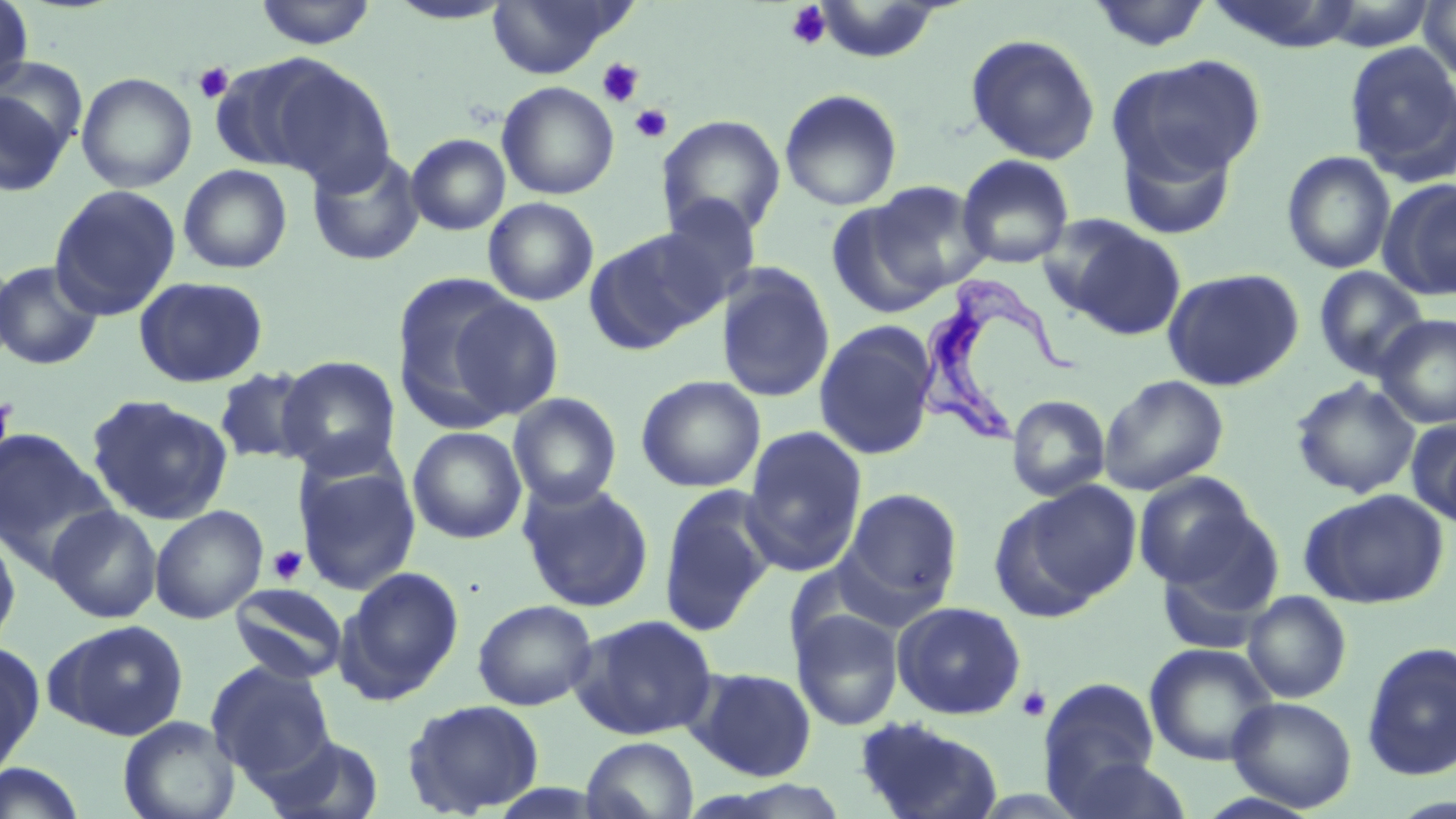
Approximate bounding boxes as (x1,y1)-(x2,y2) corner pairs in pixels. Platelet locations: (784,2)-(832,51), (597,57)-(644,107), (193,62)-(234,103), (630,104)-(672,143), (0,391)-(15,463), (266,545)-(308,586), (1016,686)-(1051,722). Trypanosoma brucei locations: (911,271)-(1082,446). Uninfected red blood cell locations: (1,0)-(34,95), (811,0)-(948,63), (1088,0)-(1214,53), (1418,0)-(1456,81), (254,1)-(377,49), (385,1)-(516,25), (486,1)-(631,79), (1315,1)-(1438,50), (964,33)-(1101,165), (1343,41)-(1456,185), (237,53)-(395,189), (1111,54)-(1266,185), (76,72)-(197,193), (497,81)-(620,200), (0,83)-(73,198), (779,88)-(903,211), (657,115)-(787,240), (1115,126)-(1240,241), (405,133)-(511,236), (307,148)-(425,267), (1281,151)-(1397,274), (957,154)-(1074,268), (178,164)-(293,274), (861,178)-(989,298), (1379,178)-(1456,301), (48,185)-(181,320), (656,193)-(763,311), (482,197)-(599,306), (823,197)-(952,320), (1048,217)-(1188,339), (584,228)-(719,354), (0,253)-(18,370), (0,261)-(104,371), (717,263)-(836,404), (1314,265)-(1430,380), (1162,268)-(1304,391), (390,274)-(540,430), (133,276)-(268,388), (446,296)-(563,420), (1374,314)-(1456,429), (813,320)-(939,461), (277,355)-(402,478), (213,366)-(320,465), (1098,374)-(1229,495), (636,375)-(766,493), (1290,378)-(1421,498), (508,392)-(622,509), (86,394)-(233,526), (1007,395)-(1110,502), (1407,418)-(1456,528), (0,426)-(114,571), (407,426)-(527,544), (740,426)-(867,575), (293,458)-(421,596), (1133,472)-(1263,588), (517,479)-(654,613), (994,482)-(1142,617), (657,484)-(777,636), (840,488)-(963,615), (1299,488)-(1450,609), (45,504)-(162,623), (149,505)-(268,625), (1154,512)-(1285,646), (0,524)-(22,656), (337,566)-(465,703), (230,583)-(349,684), (1242,591)-(1352,703), (471,598)-(598,711), (891,600)-(1026,720), (790,607)-(904,731), (570,614)-(719,740), (44,619)-(190,741), (1361,642)-(1456,781), (0,643)-(44,778), (1144,643)-(1278,766), (206,660)-(335,781), (687,666)-(817,781), (1038,676)-(1162,809), (1227,696)-(1357,812), (401,699)-(545,816), (117,715)-(240,819), (852,716)-(1004,819), (254,732)-(386,819), (580,736)-(699,819), (1057,754)-(1194,819), (0,762)-(88,819). Slide-level diagnosis: Trypanosoma brucei. One field of a larger specimen. Captured at 1000x magnification. Light microscopy. Thin blood film. May-Grünwald-Giemsa-stained preparation. Image is 1456×819 pixels.